Assess this cell for malaria.
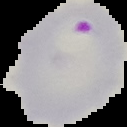

Parasitized.

Image is 127×127 pixels. Cell region segmented out of the field of view; the surrounding area is masked to black. From a thin blood smear.